Comment on the morphology of the red blood cells.
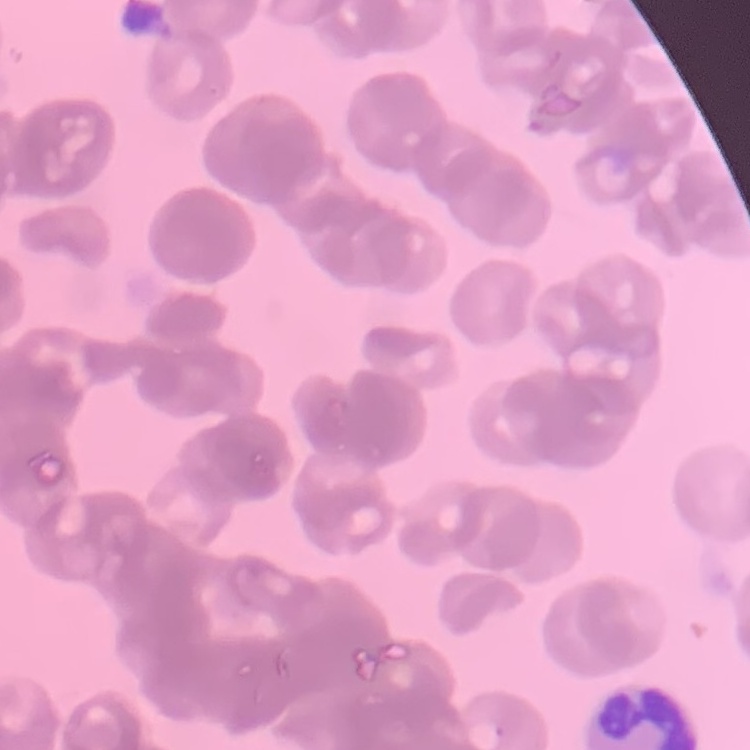
They show rouleaux formation.

stain = Field's or Giemsa
preparation = thin blood film
image type = square crop of a larger photomicrograph